State the preparation type.
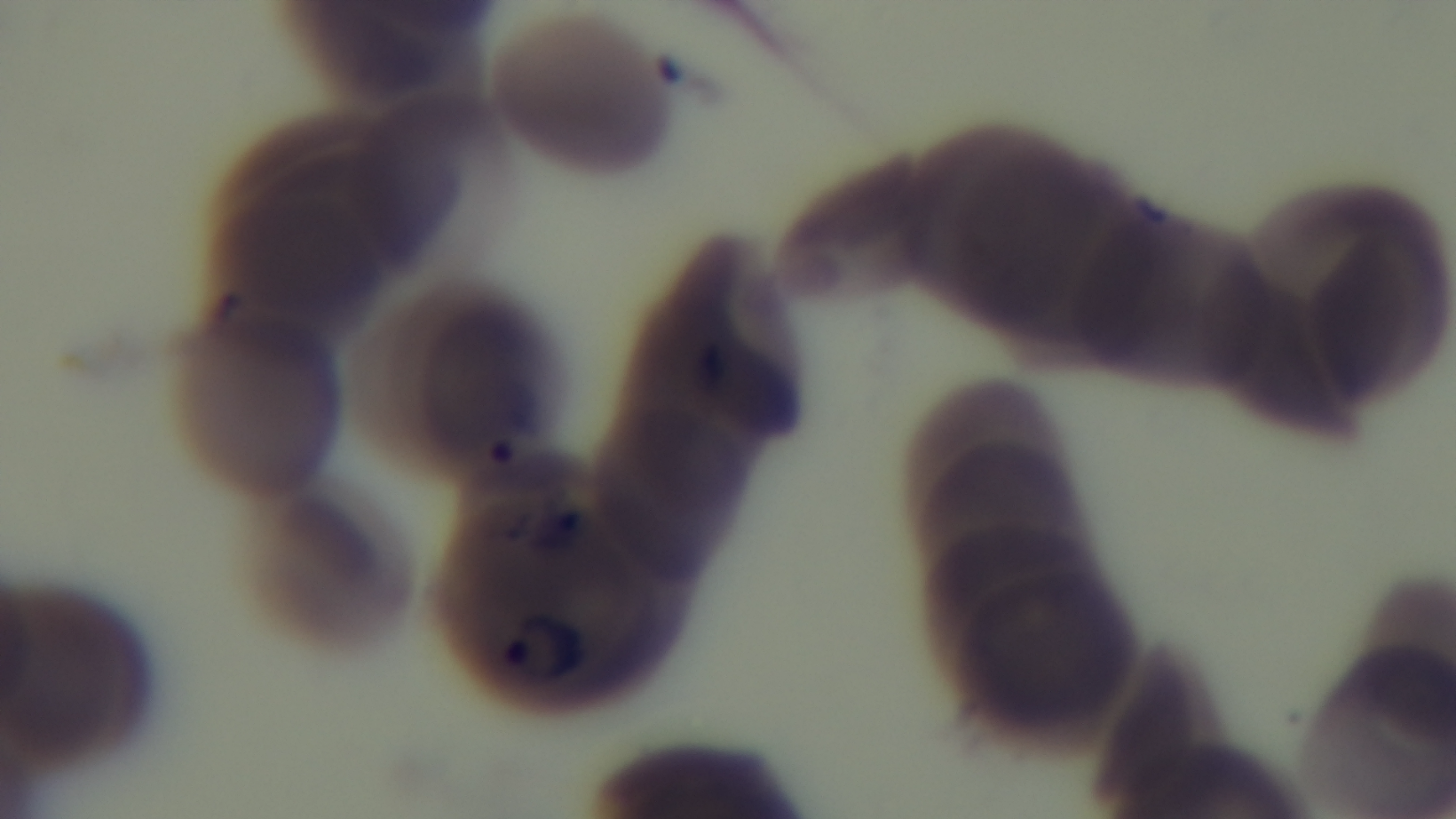
Thin.

malaria status = infected
objective = 100x oil immersion
field of view = one from the slide
modality = light microscopy
stain = Giemsa
capture = mounted 4K digital camera